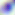 Toxoplasma gondii is shown. 400x magnification. Micrograph.